Find the cells and give the type of each one.
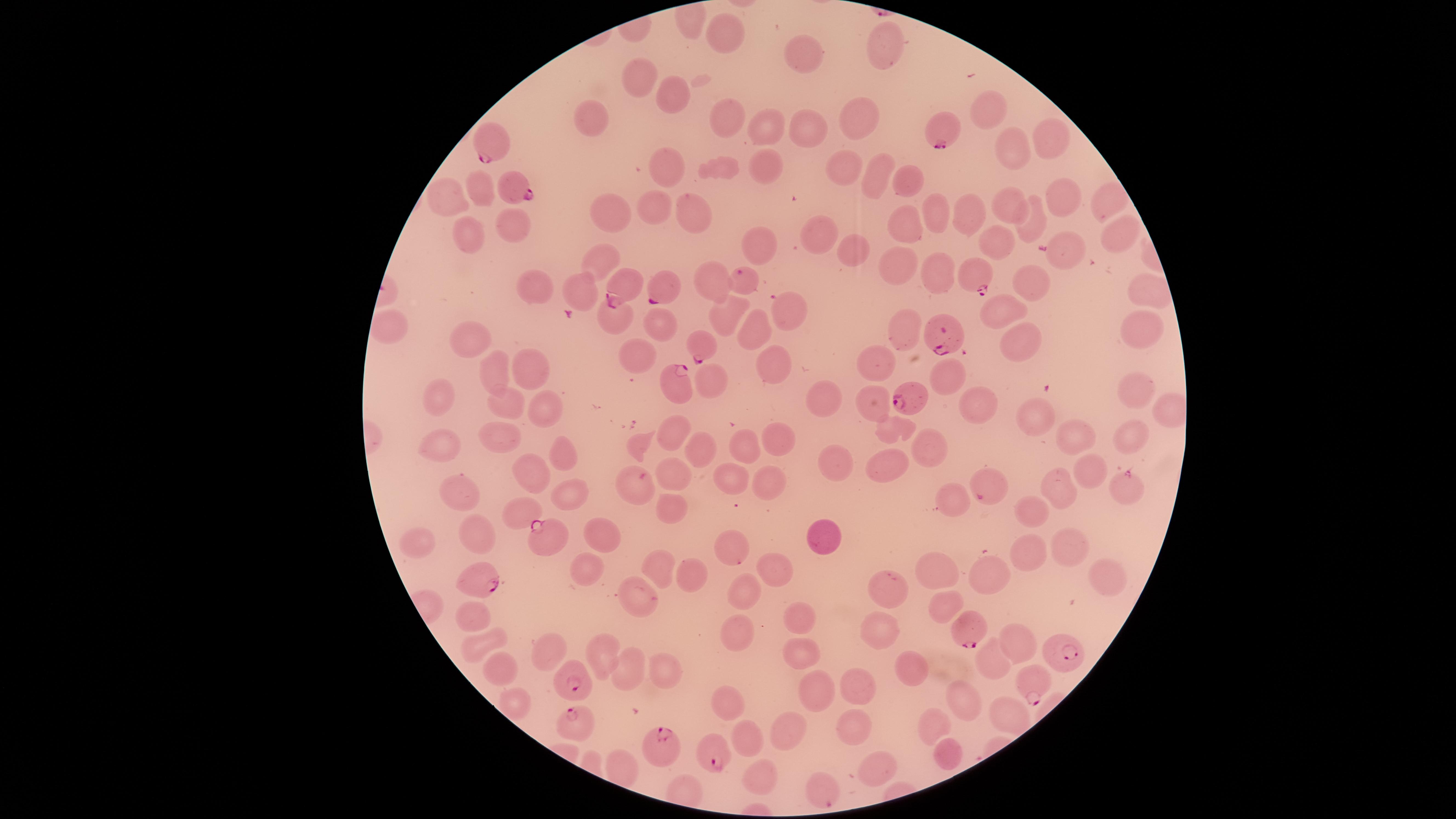
Approximate marker points as {x, y} in pixels.
Parasitized RBCs: {944, 128}, {492, 142}, {512, 190}, {976, 277}, {742, 280}, {627, 289}, {658, 290}, {787, 309}, {945, 331}, {701, 346}, {679, 387}, {912, 396}, {1128, 486}, {986, 489}, {548, 539}, {733, 550}, {481, 580}, {969, 630}, {1068, 650}, {574, 681}, {1036, 685}, {576, 718}, {715, 752}, {662, 753}, {821, 790}.
Uninfected RBCs: {731, 30}, {883, 48}, {805, 52}, {632, 72}, {676, 92}, {988, 109}, {589, 117}, {728, 119}, {806, 126}, {861, 126}, {765, 129}, {1052, 135}, {1012, 147}, {768, 167}, {720, 170}, {671, 171}, {848, 171}, {873, 177}, {910, 177}, {484, 187}, {1103, 192}, {452, 193}, {1060, 196}, {1014, 204}, {654, 207}, {934, 211}, {619, 213}, {964, 213}, {697, 215}, {1039, 224}, {516, 228}, {908, 228}, {1114, 232}, {469, 234}, {825, 238}, {1002, 240}, {765, 246}, {1068, 250}, {857, 253}, {603, 261}, {931, 269}, {898, 270}, {706, 276}, {1036, 283}, {1142, 289}, {586, 292}, {534, 293}, {730, 311}, {618, 315}, {1007, 317}, {660, 320}, {753, 323}, {1138, 326}, {392, 328}, {907, 333}, {474, 340}, {1022, 349}, {640, 353}, {774, 362}, {876, 369}, {532, 371}, {495, 373}, {719, 375}, {954, 379}, {1131, 388}, {822, 392}, {437, 397}, {976, 402}, {542, 404}, {872, 404}, {506, 405}, {1036, 419}, {898, 425}, {677, 430}, {501, 432}, {776, 432}, {1078, 436}, {1131, 437}, {642, 439}, {744, 442}, {927, 443}, {440, 449}, {562, 451}, {704, 452}, {839, 461}, {678, 470}, {887, 470}, {535, 474}, {1093, 475}, {771, 476}, {637, 478}, {726, 478}, {1060, 487}, {460, 490}, {571, 492}, {956, 492}, {523, 507}, {676, 510}, {1035, 514}, {477, 530}, {602, 531}, {821, 534}, {421, 544}, {1069, 544}, {1029, 551}, {583, 567}, {943, 567}, {776, 568}, {661, 572}, {990, 574}, {695, 576}, {1100, 576}, {889, 588}, {742, 596}, {645, 598}, {949, 604}, {474, 612}, {798, 622}, {879, 630}, {741, 637}, {1018, 639}, {553, 641}, {479, 642}, {804, 647}, {601, 657}, {996, 662}, {499, 663}, {907, 665}, {661, 670}, {627, 674}, {808, 686}, {860, 689}, {728, 698}, {968, 700}, {513, 703}, {1002, 712}, {853, 722}, {927, 725}, {783, 731}, {755, 734}, {950, 752}, {616, 768}, {883, 772}, {758, 775}.
No WBCs identified.

Summary:
  - Field of view: single
  - Image size: 1456×819 pixels
  - Preparation: thin blood smear
  - Capture: smartphone photograph through the microscope eyepiece
  - Stain: Giemsa
  - Species: Plasmodium falciparum
  - Visible region: circular